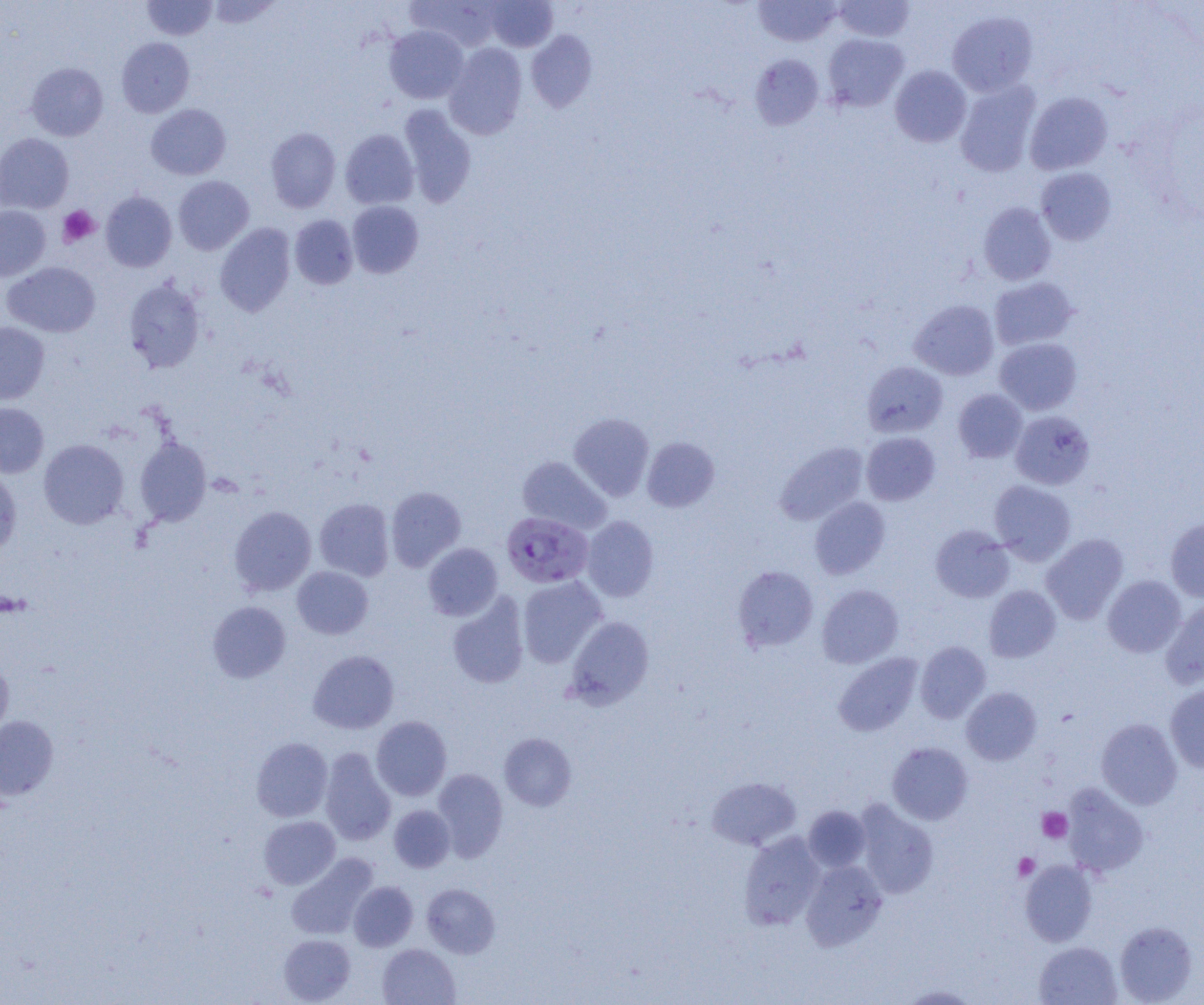

slide_level_diagnosis: Plasmodium falciparum
preparation: thin blood smear
modality: optical microscopy
field_of_view: single
uninfected_red_blood_cell_locations: 'approximate bounding boxes as named x1/y1/x2/y2 corners in pixels: (x1=142, y1=0, x2=216, y2=40), (x1=205, y1=0, x2=281, y2=29), (x1=407, y1=0, x2=502, y2=51), (x1=753, y1=0, x2=843, y2=46), (x1=833, y1=0, x2=916, y2=42), (x1=485, y1=1, x2=558, y2=52), (x1=947, y1=11, x2=1038, y2=97), (x1=384, y1=25, x2=469, y2=104), (x1=526, y1=30, x2=597, y2=113), (x1=822, y1=33, x2=909, y2=112), (x1=116, y1=37, x2=194, y2=118), (x1=443, y1=43, x2=527, y2=140), (x1=750, y1=53, x2=824, y2=130), (x1=26, y1=62, x2=108, y2=141), (x1=889, y1=65, x2=971, y2=147), (x1=955, y1=80, x2=1041, y2=177), (x1=1025, y1=92, x2=1112, y2=175), (x1=146, y1=104, x2=231, y2=179), (x1=398, y1=105, x2=477, y2=207), (x1=265, y1=127, x2=341, y2=212), (x1=340, y1=129, x2=419, y2=209), (x1=0, y1=133, x2=74, y2=213), (x1=1036, y1=167, x2=1116, y2=245), (x1=173, y1=176, x2=254, y2=255), (x1=101, y1=191, x2=177, y2=272), (x1=347, y1=200, x2=424, y2=278), (x1=978, y1=202, x2=1056, y2=286), (x1=0, y1=206, x2=51, y2=281), (x1=289, y1=215, x2=358, y2=289), (x1=215, y1=223, x2=296, y2=316), (x1=2, y1=262, x2=101, y2=337), (x1=989, y1=277, x2=1078, y2=350), (x1=123, y1=278, x2=206, y2=373), (x1=909, y1=299, x2=999, y2=380), (x1=0, y1=322, x2=49, y2=404), (x1=994, y1=337, x2=1082, y2=415), (x1=863, y1=361, x2=948, y2=437), (x1=953, y1=389, x2=1027, y2=463), (x1=0, y1=403, x2=48, y2=477), (x1=1010, y1=411, x2=1094, y2=489), (x1=569, y1=412, x2=654, y2=501), (x1=861, y1=432, x2=940, y2=505), (x1=135, y1=436, x2=211, y2=525), (x1=642, y1=437, x2=719, y2=512), (x1=39, y1=439, x2=128, y2=529), (x1=775, y1=441, x2=868, y2=525), (x1=517, y1=456, x2=611, y2=534), (x1=0, y1=466, x2=21, y2=557), (x1=989, y1=480, x2=1076, y2=564), (x1=386, y1=486, x2=466, y2=571), (x1=810, y1=497, x2=890, y2=579), (x1=314, y1=498, x2=394, y2=581), (x1=229, y1=506, x2=317, y2=596), (x1=581, y1=515, x2=659, y2=602), (x1=1165, y1=519, x2=1204, y2=602), (x1=930, y1=525, x2=1014, y2=602), (x1=1041, y1=534, x2=1128, y2=624), (x1=423, y1=543, x2=503, y2=620), (x1=292, y1=566, x2=373, y2=639), (x1=733, y1=566, x2=818, y2=652), (x1=1102, y1=575, x2=1185, y2=657), (x1=517, y1=576, x2=607, y2=668), (x1=817, y1=584, x2=904, y2=668), (x1=983, y1=585, x2=1061, y2=662), (x1=447, y1=594, x2=529, y2=689), (x1=1160, y1=600, x2=1204, y2=689), (x1=207, y1=601, x2=291, y2=683), (x1=565, y1=616, x2=654, y2=709), (x1=915, y1=641, x2=991, y2=723), (x1=308, y1=650, x2=399, y2=734), (x1=833, y1=653, x2=923, y2=736), (x1=0, y1=659, x2=13, y2=742), (x1=1165, y1=684, x2=1204, y2=773), (x1=961, y1=687, x2=1042, y2=765), (x1=0, y1=716, x2=58, y2=799), (x1=371, y1=716, x2=452, y2=801), (x1=1096, y1=718, x2=1182, y2=809), (x1=499, y1=732, x2=577, y2=810), (x1=251, y1=737, x2=333, y2=822), (x1=887, y1=742, x2=973, y2=824), (x1=319, y1=747, x2=396, y2=846), (x1=432, y1=768, x2=508, y2=861), (x1=707, y1=776, x2=801, y2=850), (x1=1062, y1=784, x2=1149, y2=877), (x1=854, y1=800, x2=938, y2=898), (x1=389, y1=805, x2=455, y2=872), (x1=804, y1=805, x2=871, y2=872), (x1=259, y1=816, x2=340, y2=889), (x1=738, y1=831, x2=825, y2=930), (x1=287, y1=854, x2=378, y2=940), (x1=801, y1=860, x2=887, y2=951), (x1=1020, y1=860, x2=1098, y2=946), (x1=348, y1=881, x2=418, y2=951), (x1=422, y1=883, x2=500, y2=958), (x1=1114, y1=921, x2=1197, y2=1004), (x1=279, y1=934, x2=355, y2=1004), (x1=1034, y1=941, x2=1122, y2=1005), (x1=378, y1=943, x2=460, y2=1005), (x1=898, y1=985, x2=981, y2=1004)'
platelet_locations: 'approximate bounding boxes as named x1/y1/x2/y2 corners in pixels: (x1=58, y1=205, x2=100, y2=247), (x1=1037, y1=807, x2=1072, y2=843), (x1=1013, y1=853, x2=1039, y2=881)'
magnification: 1000x
image_size: 1204×1005 pixels
plasmodium_falciparum_infected_red_blood_cell_locations: 'approximate bounding boxes as named x1/y1/x2/y2 corners in pixels: (x1=507, y1=513, x2=600, y2=590)'